State which cell type is depicted.
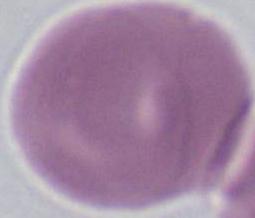
This is an erythrocyte.

Summary:
  - Magnification: 1000x
  - Modality: micrograph